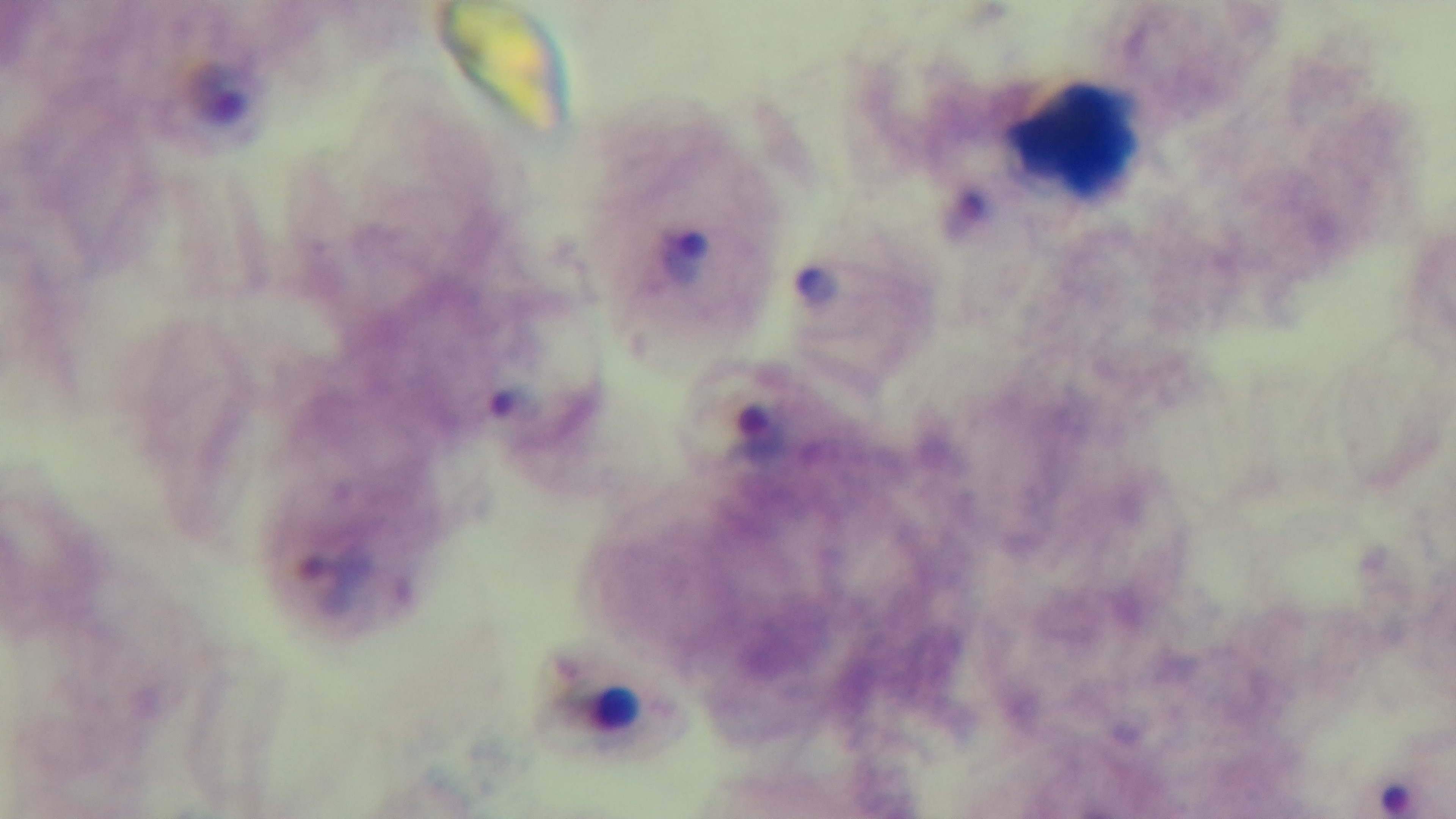 Mounted 4K digital camera. Giemsa stain. Light microscopy. Preparation: thick. Single field of view. Oil-immersion objective, 100x. Malaria status: positive.